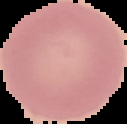 Image is 127×124 pixels. From a thin blood smear. Cell region segmented out of the field of view; the surrounding area is masked to black. Malaria status: uninfected.